Give the position of every Plasmodium parasite and every leukocyte.
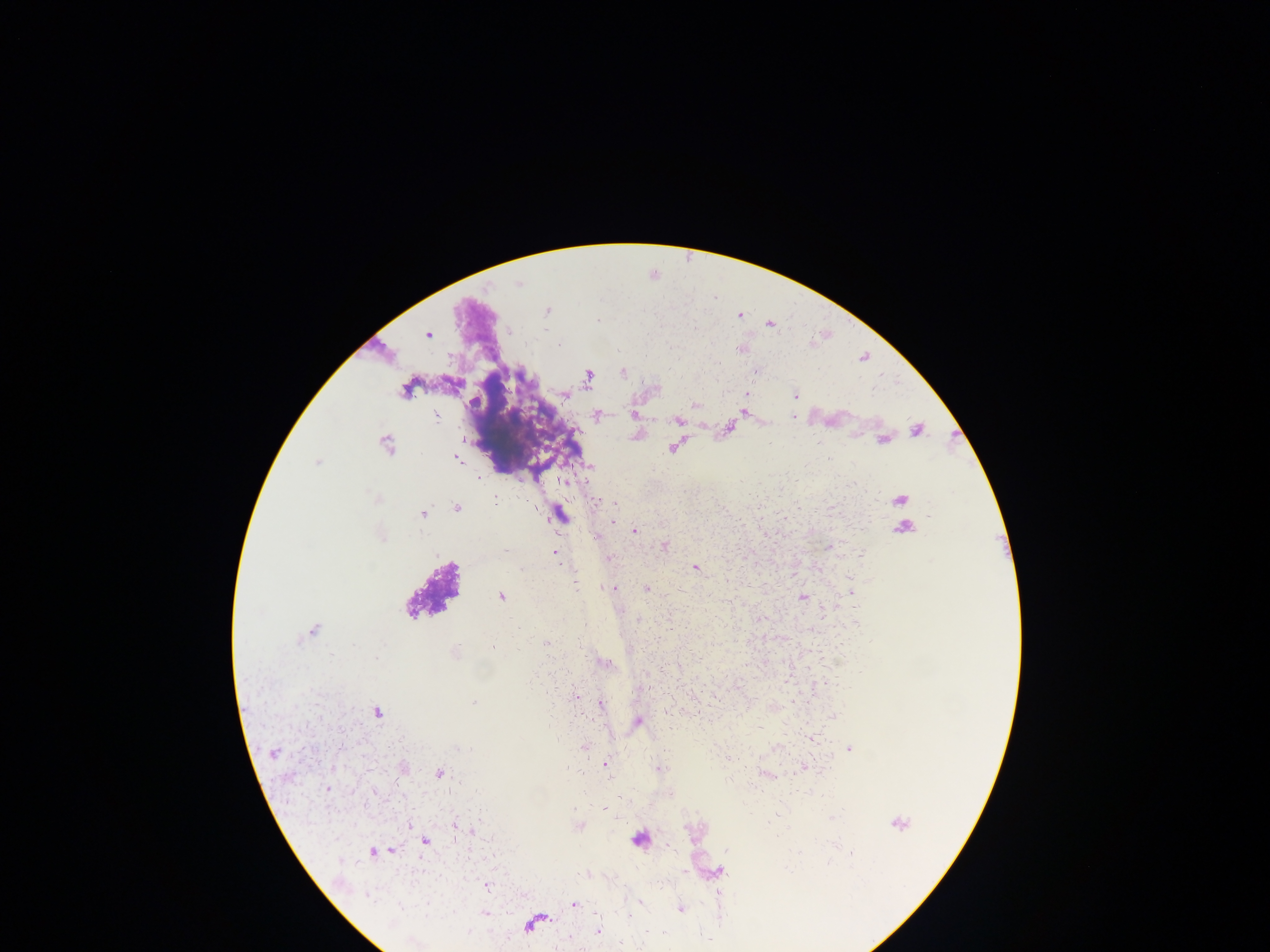
Approximate centers as x y in pixels.
Plasmodium parasites: 547 311; 740 316; 597 320; 769 325; 428 335; 739 349; 618 351; 623 373; 588 375; 405 390; 747 393; 564 395; 795 396; 695 405; 743 412; 598 415; 634 415; 437 416; 793 416; 677 421; 917 430; 883 440; 386 445; 672 448; 457 459; 317 462; 478 478; 563 481; 795 481; 376 498; 901 499; 495 501; 598 501; 614 505; 457 508; 723 509; 422 514; 560 515; 930 516; 614 520; 784 520; 903 528; 635 531; 382 536; 664 546; 828 547; 505 550; 555 553; 861 555; 609 558; 695 568; 575 583; 612 588; 646 589; 851 592; 501 596; 803 597; 638 619; 760 619; 855 622; 586 625; 811 629; 314 630; 547 643; 713 644; 841 644; 579 647; 631 650; 454 653; 664 669; 565 672; 532 678; 646 687; 575 697; 474 703; 601 704; 695 712; 377 713; 667 713; 835 714; 638 722; 811 739; 557 740; 584 746; 457 748; 468 748; 850 749; 273 753; 728 758; 606 764; 566 767; 658 768; 803 768; 403 769; 440 773; 327 789; 670 794; 619 796; 604 807; 774 816; 832 817; 770 821; 455 824; 899 825; 409 826; 579 826; 686 827; 473 832; 456 839; 425 842; 391 850; 726 850; 373 851; 852 855; 340 860; 827 864; 684 871; 582 874; 487 886; 366 896; 640 902; 573 904; 399 905; 681 909; 484 913; 629 915; 598 929; 648 931; 469 932; 662 933; 703 937; 569 938; 621 943.
No leukocytes observed.

One field of view. Collected in Ghana. Image is 1270×952 pixels. Thick blood smear. Photographed through a microscope with a mobile-phone camera.